Report the malaria status of this cell.
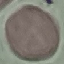

It is uninfected.

Thin smear of blood. Acquired by smartphone through the microscope eyepiece. Giemsa stain. Automatically extracted cell patch, resized to 64 × 64 pixels.